Locate every blood parasite and identify its species.
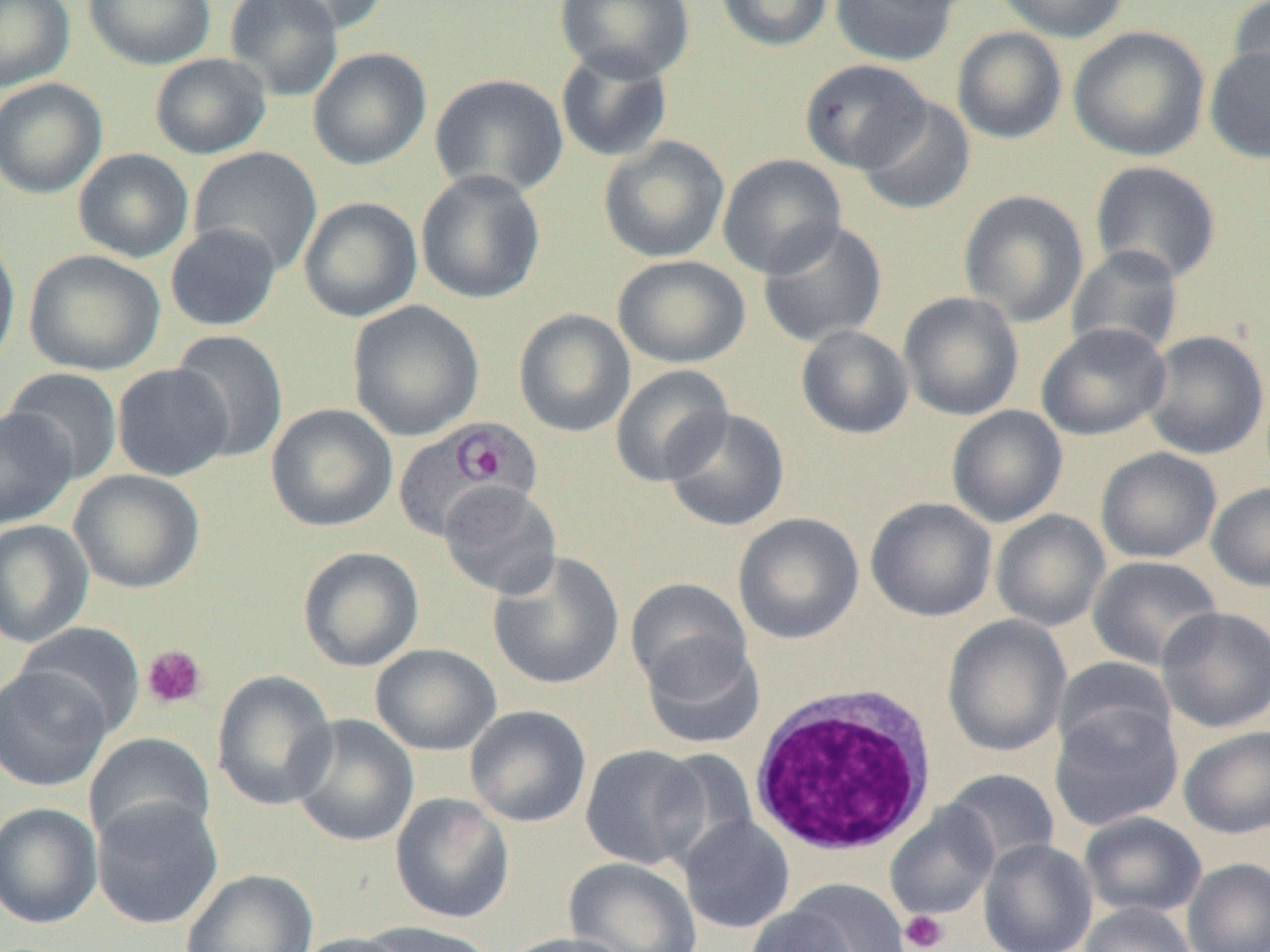

Approximate bounding boxes as [x1, y1, x2, y2] in pixels.
Plasmodium ovale-infected red blood cells: [393, 416, 543, 541].
No Plasmodium falciparum, Plasmodium malariae, Plasmodium vivax, Babesia divergens, or Trypanosoma brucei observed.

Summary:
  - Platelet locations: [141, 645, 207, 711], [900, 910, 949, 951]
  - White blood cell locations: [749, 682, 940, 861]
  - Uninfected red blood cell locations: [0, 0, 75, 92], [83, 0, 216, 70], [224, 0, 344, 101], [265, 0, 390, 36], [555, 0, 695, 82], [715, 0, 834, 52], [829, 0, 960, 67], [992, 0, 1132, 43], [1227, 0, 1270, 102], [1068, 25, 1210, 161], [951, 26, 1067, 144], [1204, 44, 1270, 164], [555, 46, 674, 163], [307, 47, 432, 170], [149, 53, 271, 159], [798, 58, 931, 174], [430, 73, 569, 198], [0, 78, 108, 198], [854, 96, 976, 215], [598, 136, 729, 263], [188, 147, 323, 275], [73, 148, 194, 263], [717, 153, 847, 279], [1089, 161, 1222, 285], [415, 169, 546, 305], [958, 189, 1089, 327], [298, 197, 423, 322], [757, 219, 888, 347], [165, 223, 282, 331], [0, 232, 21, 374], [1066, 245, 1185, 361], [24, 249, 166, 375], [613, 255, 751, 368], [898, 291, 1025, 421], [347, 300, 484, 441], [513, 308, 636, 438], [1036, 323, 1172, 441], [796, 325, 915, 439], [170, 329, 289, 463], [1142, 330, 1268, 460], [112, 363, 234, 481], [610, 364, 734, 487], [3, 368, 123, 483], [265, 404, 398, 532], [946, 405, 1068, 528], [0, 407, 77, 529], [662, 408, 791, 532], [1095, 447, 1222, 563], [69, 469, 205, 594], [1206, 482, 1270, 592], [439, 483, 562, 599], [865, 497, 997, 622], [991, 509, 1110, 632], [732, 512, 864, 644], [0, 520, 94, 648], [297, 546, 424, 672], [487, 550, 625, 690], [1086, 555, 1223, 671], [625, 579, 753, 696], [1157, 606, 1270, 733], [942, 615, 1072, 757], [13, 621, 146, 737], [639, 637, 767, 749], [370, 643, 502, 756], [1053, 657, 1177, 763], [0, 664, 113, 792], [211, 670, 338, 811], [1049, 703, 1183, 831], [464, 705, 591, 828], [288, 714, 419, 847], [1178, 725, 1270, 839], [84, 732, 216, 849], [580, 744, 710, 870], [653, 747, 761, 869], [941, 769, 1060, 870], [390, 792, 514, 924], [91, 797, 223, 929], [0, 802, 103, 930], [885, 804, 1000, 921], [1078, 812, 1207, 919], [679, 815, 796, 934], [978, 838, 1098, 952], [563, 857, 702, 952], [1182, 858, 1270, 952], [181, 868, 318, 952], [775, 880, 909, 952], [1080, 902, 1196, 952], [745, 903, 863, 952], [357, 920, 499, 952], [291, 932, 412, 952], [498, 933, 634, 952]
  - Slide-level diagnosis: Plasmodium ovale
  - Field of view: one of a larger specimen
  - Image size: 1270×952 pixels
  - Modality: light microscopy
  - Preparation: thin blood film
  - Magnification: 1000x